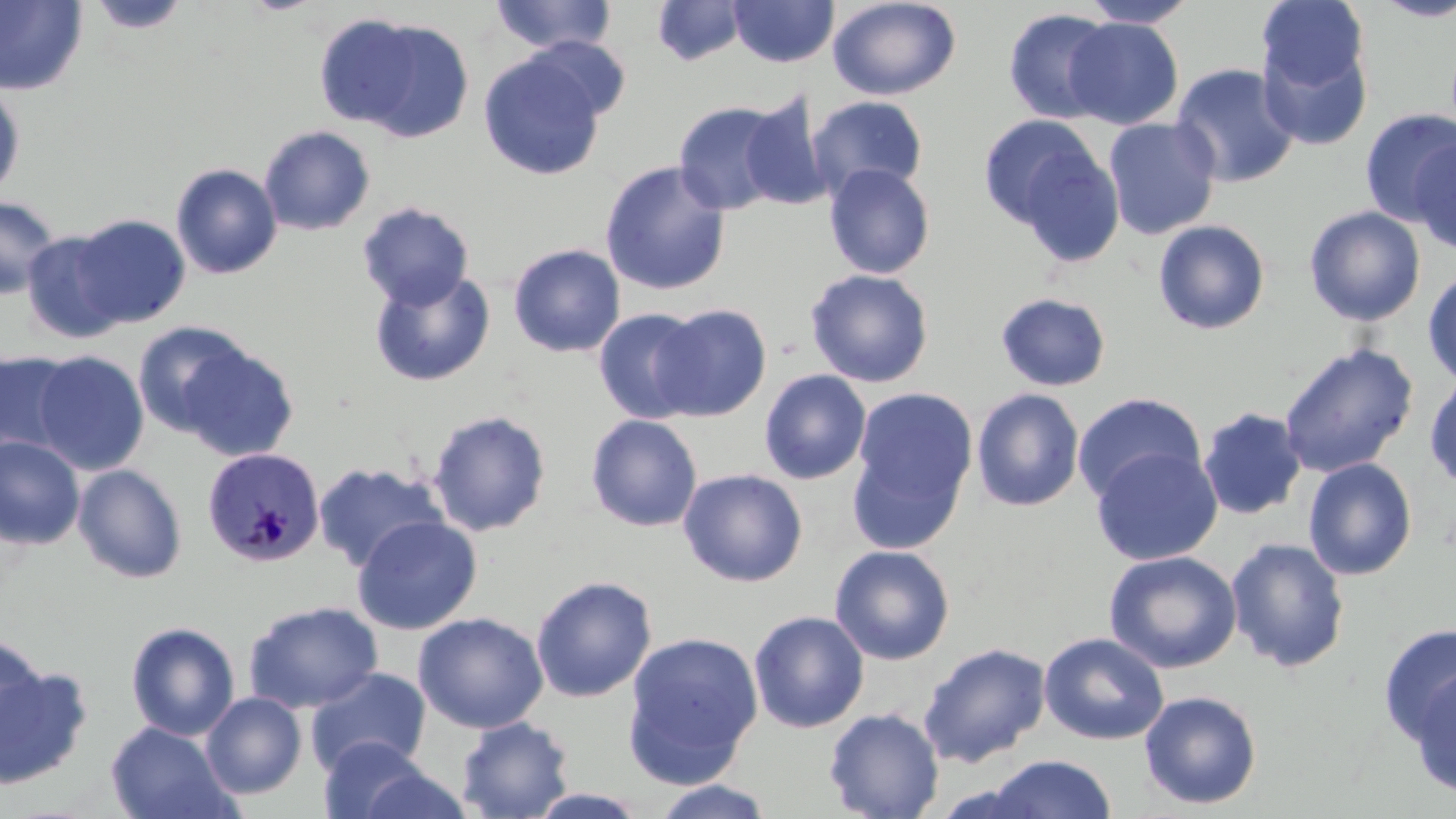

Summary:
  - Coordinate format: approximate bounding boxes as [x1, y1, x2, y2] in pixels
  - Plasmodium malariae-infected red blood cell locations: [201, 446, 326, 567]
  - Uninfected red blood cell locations: [490, 0, 616, 55], [827, 0, 961, 101], [1080, 0, 1198, 28], [1372, 0, 1456, 22], [0, 1, 88, 96], [87, 1, 191, 35], [652, 1, 748, 66], [728, 1, 839, 68], [1257, 1, 1369, 92], [1003, 7, 1118, 124], [339, 16, 475, 142], [1063, 17, 1184, 130], [525, 36, 633, 122], [1258, 40, 1373, 151], [478, 52, 606, 181], [1170, 63, 1301, 188], [0, 84, 26, 202], [738, 95, 833, 210], [807, 95, 928, 201], [672, 100, 790, 216], [1358, 108, 1456, 227], [977, 114, 1104, 232], [1103, 117, 1221, 240], [259, 125, 375, 236], [1007, 137, 1127, 270], [1409, 138, 1456, 255], [600, 160, 731, 296], [170, 163, 283, 280], [823, 163, 936, 279], [0, 195, 61, 300], [357, 202, 475, 310], [1304, 205, 1426, 326], [69, 214, 190, 328], [1152, 219, 1272, 336], [22, 231, 128, 345], [508, 243, 626, 358], [369, 268, 496, 387], [805, 268, 934, 388], [1423, 268, 1456, 388], [995, 292, 1112, 391], [651, 303, 772, 421], [593, 308, 707, 423], [132, 320, 254, 439], [1277, 342, 1419, 478], [178, 343, 299, 463], [0, 350, 78, 458], [32, 351, 150, 475], [759, 369, 871, 484], [1424, 372, 1456, 491], [851, 386, 978, 521], [971, 388, 1085, 512], [1072, 392, 1207, 506], [1197, 406, 1308, 520], [427, 409, 552, 537], [585, 414, 703, 532], [0, 436, 85, 550], [845, 440, 968, 558], [1090, 446, 1223, 566], [1302, 457, 1418, 581], [312, 462, 448, 573], [73, 463, 188, 583], [678, 468, 808, 587], [352, 514, 482, 635], [1225, 537, 1350, 673], [829, 544, 955, 665], [1103, 550, 1242, 673], [530, 575, 657, 702], [243, 600, 383, 714], [748, 610, 869, 733], [412, 612, 549, 734], [126, 621, 240, 740], [1378, 623, 1456, 748], [621, 631, 763, 786], [1039, 632, 1170, 745], [0, 634, 47, 745], [918, 642, 1051, 768], [0, 665, 94, 790], [1404, 666, 1455, 797], [304, 667, 432, 778], [1138, 690, 1263, 810], [201, 692, 307, 799], [823, 707, 945, 819], [455, 715, 576, 819], [106, 721, 239, 819], [316, 735, 433, 818], [984, 754, 1117, 818], [355, 765, 475, 818], [651, 780, 775, 818], [523, 787, 651, 817]
  - Slide-level diagnosis: Plasmodium malariae
  - Field of view: one of a larger specimen
  - Image size: 1456×819 pixels
  - Modality: light microscopy
  - Stain: May-Grünwald-Giemsa
  - Preparation: thin blood smear
  - Magnification: 1000x